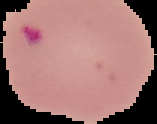
Summary:
  - Preparation: thin blood smear
  - Result: malaria parasites detected
  - Image type: segmented cell region with the area outside set to black
  - Image size: 157×124 pixels